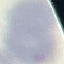

Summary:
  - Malaria status: uninfected
  - Capture: smartphone camera at the microscope eyepiece
  - Preparation: thin smear
  - Stain: Giemsa
  - Image type: cell patch, automatically extracted from a larger field of view and resized to 64 × 64 pixels